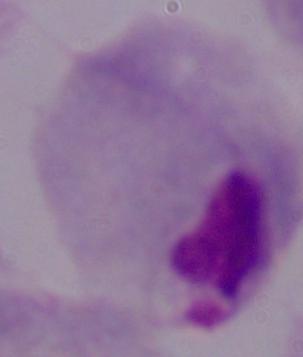
modality = micrograph
identification = trichomonad
magnification = 1000x